Classify this cell by malaria status.
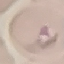

It is parasitized.

Cell patch, automatically extracted from a larger field of view and resized to 64 × 64 pixels. Thin smear of blood. Acquired by smartphone through the microscope eyepiece. Giemsa-stained preparation.